Outline each blood parasite and name the species.
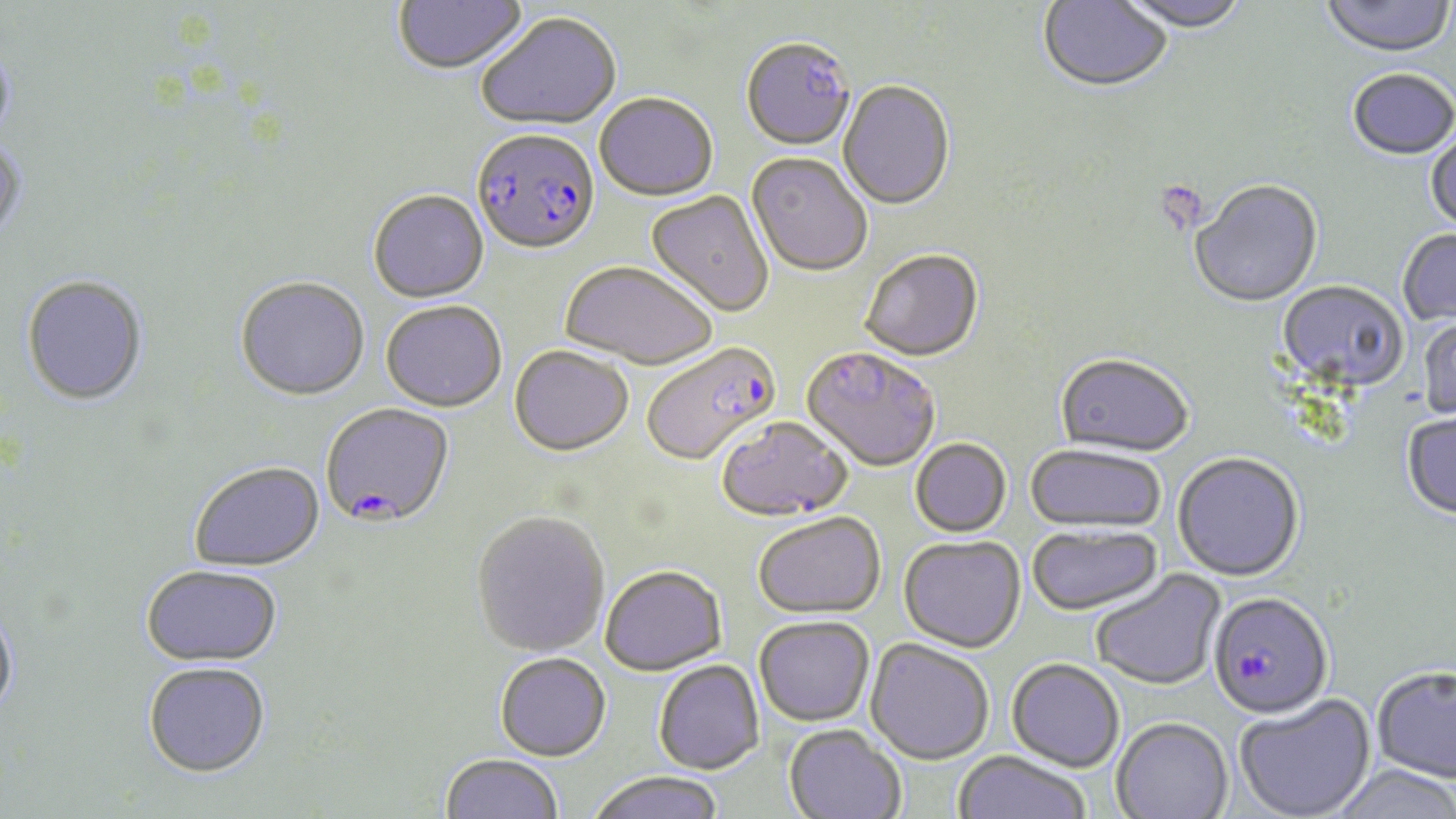

Approximate bounding boxes as [x1, y1, x2, y2] in pixels.
Plasmodium falciparum-infected red blood cells: [472, 130, 600, 258], [642, 343, 781, 467], [801, 348, 940, 473], [320, 404, 455, 530], [1207, 592, 1334, 720].
No Plasmodium ovale, Plasmodium malariae, Plasmodium vivax, Babesia divergens, or Trypanosoma brucei observed.

Summary:
  - Uninfected red blood cell locations: [393, 0, 528, 77], [1037, 0, 1173, 95], [1115, 0, 1250, 35], [1320, 0, 1455, 59], [476, 14, 621, 133], [0, 37, 16, 148], [741, 41, 856, 153], [1348, 71, 1456, 162], [838, 81, 955, 212], [594, 94, 718, 202], [1425, 128, 1456, 235], [0, 140, 28, 243], [746, 154, 872, 278], [1190, 181, 1323, 309], [368, 191, 489, 304], [645, 191, 774, 318], [1397, 229, 1456, 328], [859, 250, 984, 364], [560, 263, 718, 372], [21, 276, 149, 408], [235, 278, 370, 402], [1276, 281, 1408, 394], [380, 302, 507, 413], [1418, 314, 1456, 422], [510, 347, 634, 457], [1055, 355, 1194, 459], [1401, 413, 1456, 522], [716, 417, 852, 522], [910, 439, 1011, 537], [1025, 444, 1166, 534], [1173, 452, 1304, 582], [189, 463, 325, 574], [471, 512, 610, 657], [753, 512, 886, 619], [1026, 523, 1163, 616], [898, 536, 1025, 653], [141, 565, 283, 667], [600, 565, 727, 676], [1091, 569, 1226, 691], [0, 604, 19, 720], [754, 616, 874, 726], [865, 639, 994, 765], [494, 652, 611, 761], [1006, 658, 1125, 772], [653, 660, 764, 775], [143, 661, 271, 778], [1372, 665, 1456, 783], [1234, 694, 1376, 819], [1112, 717, 1234, 819], [784, 724, 906, 819], [952, 751, 1092, 819], [440, 754, 564, 819], [1328, 764, 1456, 819], [586, 771, 725, 819]
  - Platelet locations: [1153, 180, 1210, 234]
  - Slide-level diagnosis: Plasmodium falciparum
  - Modality: optical microscopy
  - Stain: May-Grünwald-Giemsa
  - Field of view: one of a larger specimen
  - Image size: 1456×819 pixels
  - Magnification: 1000x
  - Preparation: thin blood film